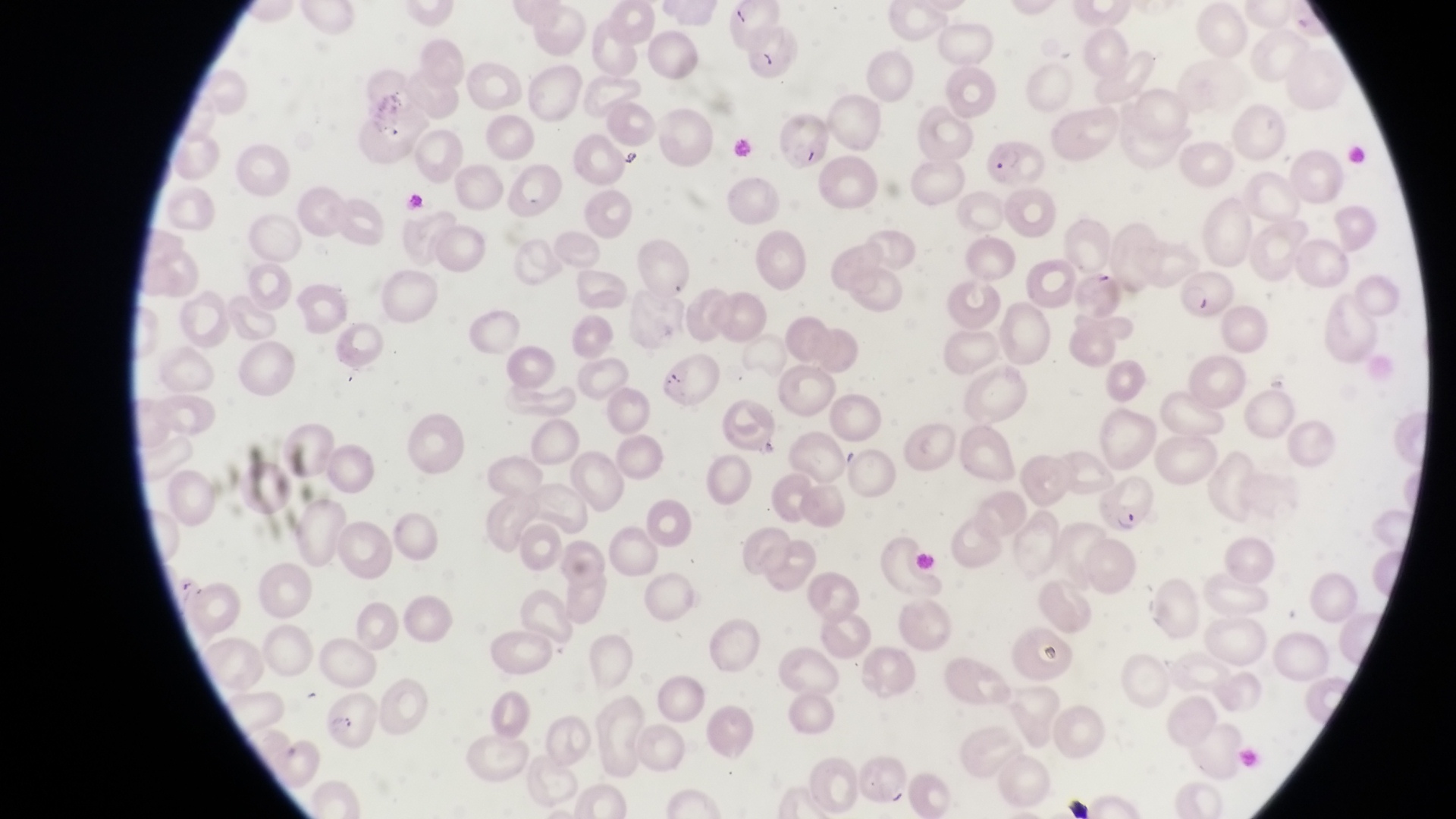

{
  "magnification": "1000x",
  "artifact_platelet_like_body_stain_precipitate_or_debris_locations": "approximate bounding boxes as (left, top, right, bottom) in pixels: (730, 3, 754, 27), (758, 47, 779, 73), (617, 148, 641, 169), (660, 357, 689, 390), (1034, 632, 1067, 669)",
  "capture": "smartphone photograph through the eyepiece of an Olympus CX-23 microscope",
  "parasitised_red_blood_cell_locations": "approximate bounding boxes as (left, top, right, bottom) in pixels: (779, 109, 828, 164), (986, 136, 1049, 188), (1175, 264, 1234, 317), (1099, 475, 1158, 539)",
  "image_size": "1456×819 pixels",
  "preparation": "thin blood film",
  "country": "Uganda",
  "field_of_view": "single"
}